Locate every blood parasite and identify its species.
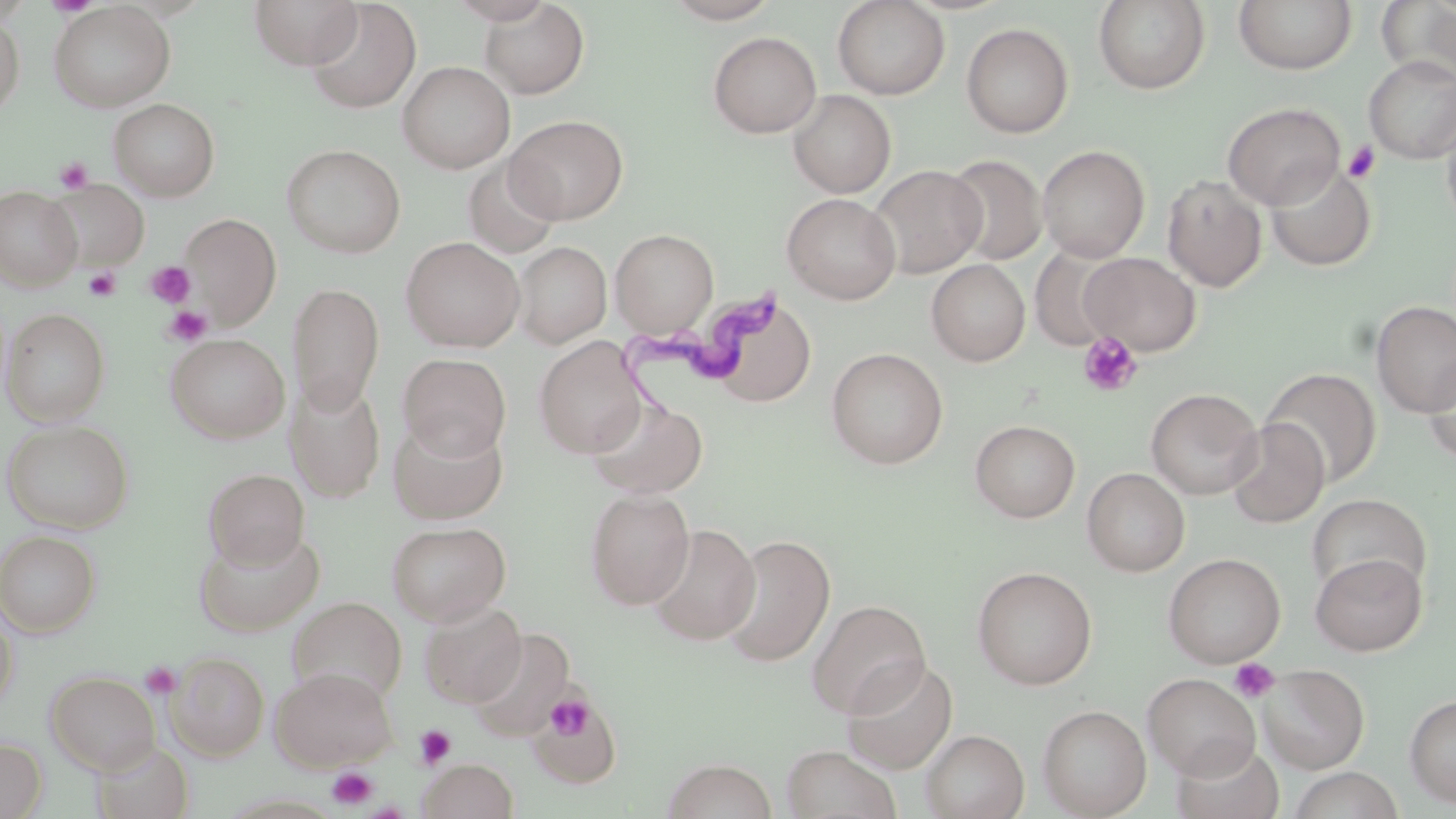
Approximate bounding boxes as named x1/y1/x2/y2 corners in pixels.
Trypanosoma brucei: (x1=619, y1=288, x2=780, y2=422).
No Plasmodium falciparum, Plasmodium ovale, Plasmodium malariae, Plasmodium vivax, or Babesia divergens observed.

Summary:
  - Platelet locations: (x1=1342, y1=141, x2=1382, y2=184), (x1=54, y1=156, x2=94, y2=193), (x1=144, y1=260, x2=195, y2=308), (x1=83, y1=267, x2=122, y2=300), (x1=163, y1=305, x2=213, y2=347), (x1=1077, y1=332, x2=1143, y2=397), (x1=1230, y1=658, x2=1280, y2=703), (x1=141, y1=662, x2=181, y2=698), (x1=531, y1=690, x2=619, y2=787), (x1=544, y1=693, x2=594, y2=741), (x1=414, y1=725, x2=456, y2=768), (x1=327, y1=766, x2=378, y2=809)
  - Uninfected red blood cell locations: (x1=248, y1=0, x2=364, y2=69), (x1=662, y1=0, x2=781, y2=24), (x1=832, y1=0, x2=950, y2=99), (x1=1092, y1=0, x2=1211, y2=94), (x1=1233, y1=0, x2=1358, y2=75), (x1=1376, y1=0, x2=1456, y2=84), (x1=48, y1=2, x2=175, y2=113), (x1=305, y1=2, x2=421, y2=114), (x1=478, y1=2, x2=590, y2=99), (x1=0, y1=10, x2=25, y2=120), (x1=961, y1=23, x2=1074, y2=138), (x1=707, y1=32, x2=821, y2=138), (x1=1364, y1=56, x2=1456, y2=164), (x1=398, y1=60, x2=515, y2=173), (x1=788, y1=90, x2=896, y2=198), (x1=109, y1=98, x2=220, y2=200), (x1=1222, y1=101, x2=1345, y2=210), (x1=1440, y1=109, x2=1456, y2=233), (x1=506, y1=115, x2=628, y2=223), (x1=281, y1=144, x2=406, y2=258), (x1=1037, y1=144, x2=1150, y2=262), (x1=945, y1=154, x2=1047, y2=266), (x1=462, y1=156, x2=564, y2=260), (x1=868, y1=164, x2=987, y2=279), (x1=1266, y1=164, x2=1376, y2=271), (x1=1162, y1=174, x2=1268, y2=292), (x1=47, y1=180, x2=149, y2=271), (x1=0, y1=186, x2=82, y2=291), (x1=782, y1=193, x2=901, y2=304), (x1=180, y1=213, x2=281, y2=323), (x1=610, y1=228, x2=718, y2=336), (x1=401, y1=236, x2=525, y2=352), (x1=512, y1=241, x2=611, y2=348), (x1=1029, y1=246, x2=1126, y2=350), (x1=1080, y1=252, x2=1201, y2=355), (x1=926, y1=259, x2=1031, y2=366), (x1=287, y1=281, x2=385, y2=414), (x1=1371, y1=300, x2=1456, y2=416), (x1=716, y1=301, x2=816, y2=408), (x1=2, y1=308, x2=110, y2=426), (x1=165, y1=333, x2=290, y2=443), (x1=534, y1=337, x2=648, y2=457), (x1=826, y1=347, x2=948, y2=469), (x1=1421, y1=351, x2=1456, y2=466), (x1=397, y1=352, x2=512, y2=460), (x1=1261, y1=367, x2=1382, y2=487), (x1=285, y1=376, x2=387, y2=502), (x1=1146, y1=388, x2=1263, y2=500), (x1=588, y1=397, x2=708, y2=499), (x1=388, y1=416, x2=509, y2=524), (x1=1225, y1=418, x2=1329, y2=529), (x1=1, y1=419, x2=134, y2=533), (x1=969, y1=419, x2=1080, y2=522), (x1=203, y1=468, x2=310, y2=568), (x1=1082, y1=468, x2=1189, y2=576), (x1=586, y1=488, x2=695, y2=609), (x1=1307, y1=493, x2=1432, y2=600), (x1=386, y1=520, x2=511, y2=626), (x1=647, y1=523, x2=760, y2=645), (x1=0, y1=529, x2=101, y2=637), (x1=192, y1=529, x2=326, y2=637), (x1=718, y1=534, x2=836, y2=668), (x1=1163, y1=552, x2=1286, y2=668), (x1=1310, y1=552, x2=1427, y2=656), (x1=972, y1=566, x2=1097, y2=690), (x1=288, y1=597, x2=407, y2=702), (x1=807, y1=599, x2=931, y2=718), (x1=419, y1=601, x2=527, y2=708), (x1=0, y1=607, x2=18, y2=709), (x1=169, y1=651, x2=269, y2=760), (x1=841, y1=657, x2=958, y2=774), (x1=1259, y1=664, x2=1369, y2=774), (x1=271, y1=665, x2=397, y2=770), (x1=45, y1=669, x2=160, y2=774), (x1=1142, y1=673, x2=1261, y2=780), (x1=526, y1=693, x2=621, y2=788), (x1=1405, y1=693, x2=1456, y2=807), (x1=1038, y1=704, x2=1152, y2=819), (x1=920, y1=729, x2=1029, y2=819), (x1=0, y1=737, x2=47, y2=818), (x1=90, y1=739, x2=195, y2=819), (x1=1171, y1=740, x2=1285, y2=819), (x1=781, y1=744, x2=902, y2=819), (x1=662, y1=758, x2=778, y2=819), (x1=417, y1=759, x2=519, y2=819), (x1=1287, y1=766, x2=1405, y2=819)
  - Slide-level diagnosis: Trypanosoma brucei
  - Image size: 1456×819 pixels
  - Stain: May-Grünwald-Giemsa
  - Magnification: 1000x
  - Modality: light microscopy
  - Field of view: one of a larger specimen
  - Preparation: thin blood film